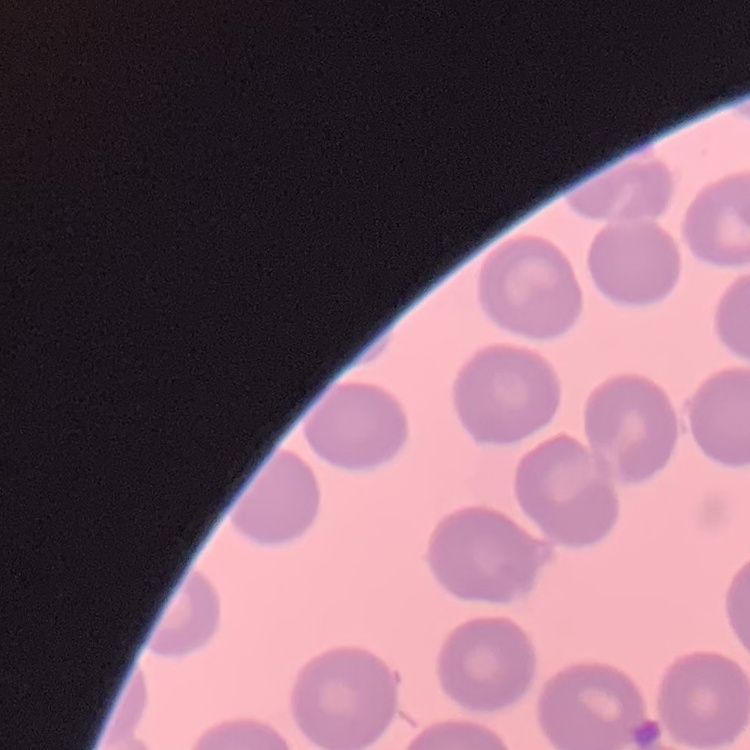

erythrocyte morphology = no rouleaux formation
stain = Field's or Giemsa
image type = one tile cut from a larger photomicrograph
preparation = thin peripheral smear